Evaluate for Plasmodium parasites.
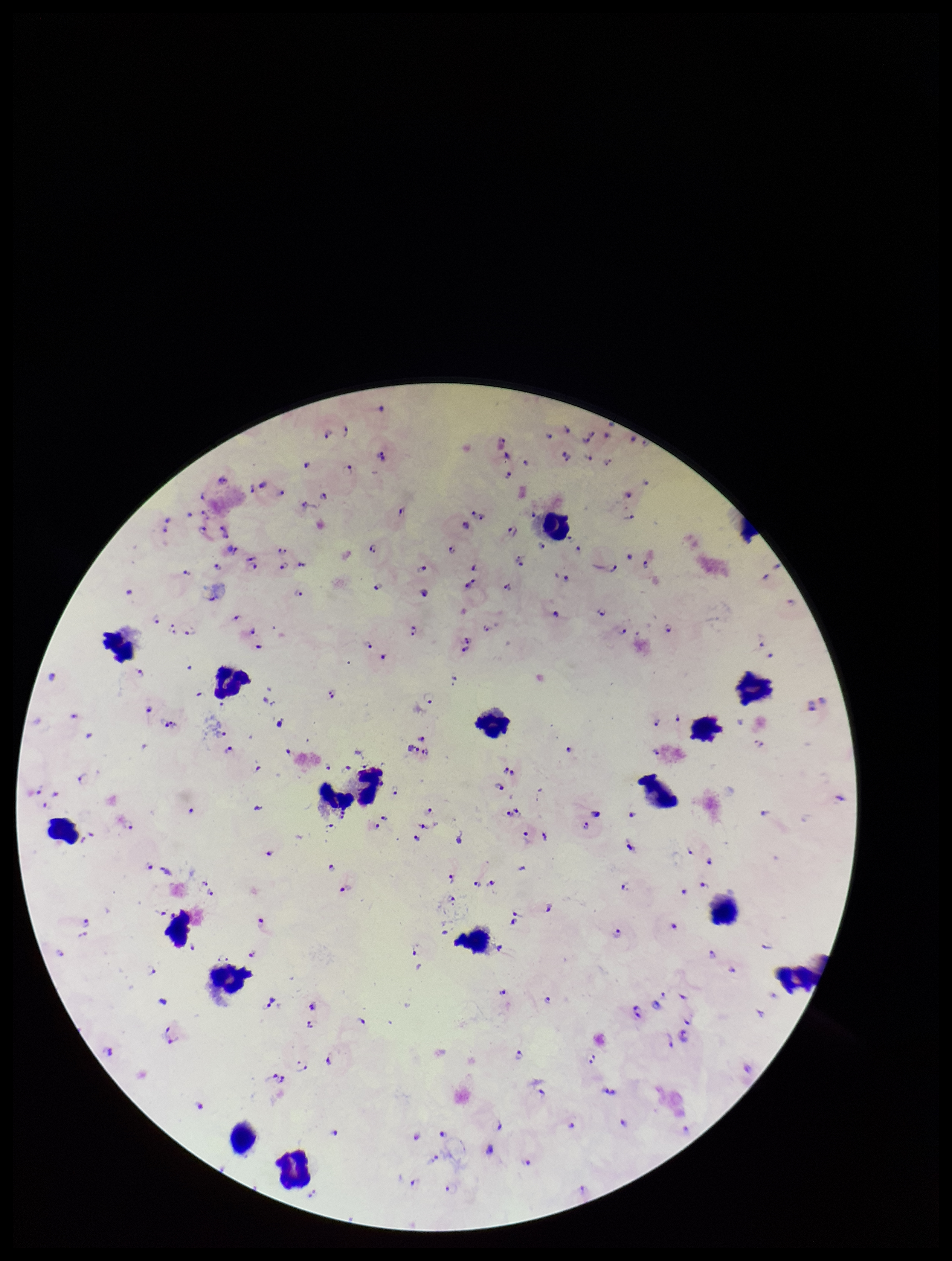

Identified.

{
  "parasite_count": 118,
  "field_of_view": "one from this slide",
  "patient_malaria_status": "infected",
  "stain": "Giemsa",
  "preparation": "thick smear",
  "leukocyte_count": 17,
  "capture": "smartphone photograph through the microscope eyepiece",
  "image_size": "952×1261 pixels",
  "species_reported_for_this_patient": "Plasmodium falciparum"
}